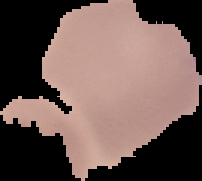
Summary:
  - Result: no Plasmodium parasites seen
  - Preparation: thin blood film
  - Image type: segmented cell region on a black background
  - Image size: 202×181 pixels